Report the malaria status of this cell.
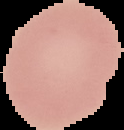
It is uninfected.

Segmented cell region on a black background. Image is 124×130 pixels. From a thin blood smear.